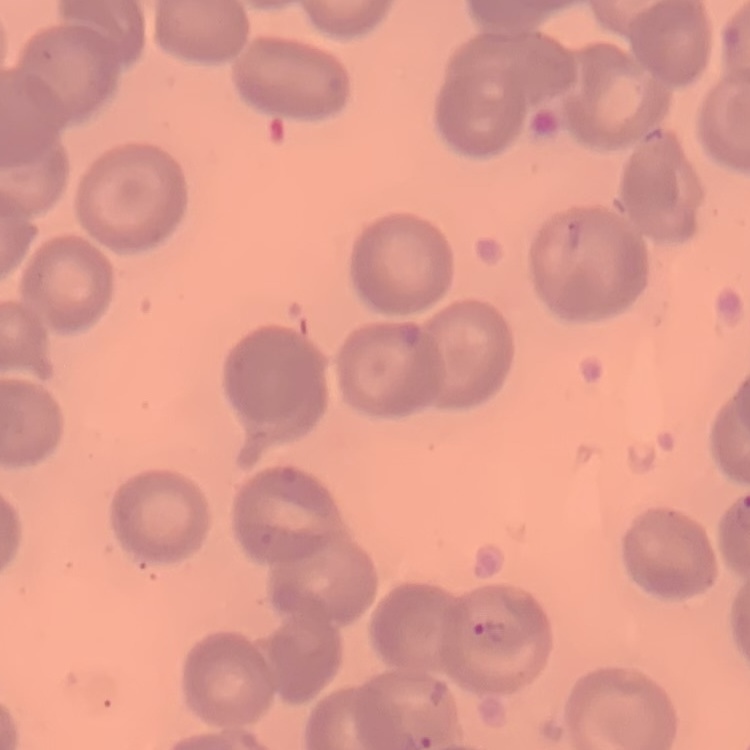
erythrocyte morphology = no rouleaux formation
preparation = thin peripheral smear
stain = Field's or Giemsa
image type = one tile cut from a larger photomicrograph